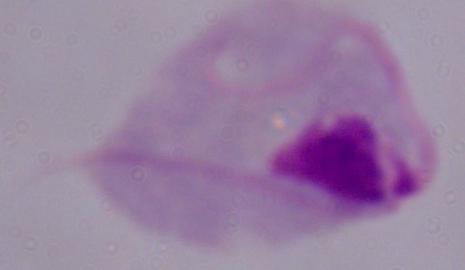 Captured at 1000x magnification. A trichomonad is shown. Micrograph.